Comment on the morphology of the erythrocytes.
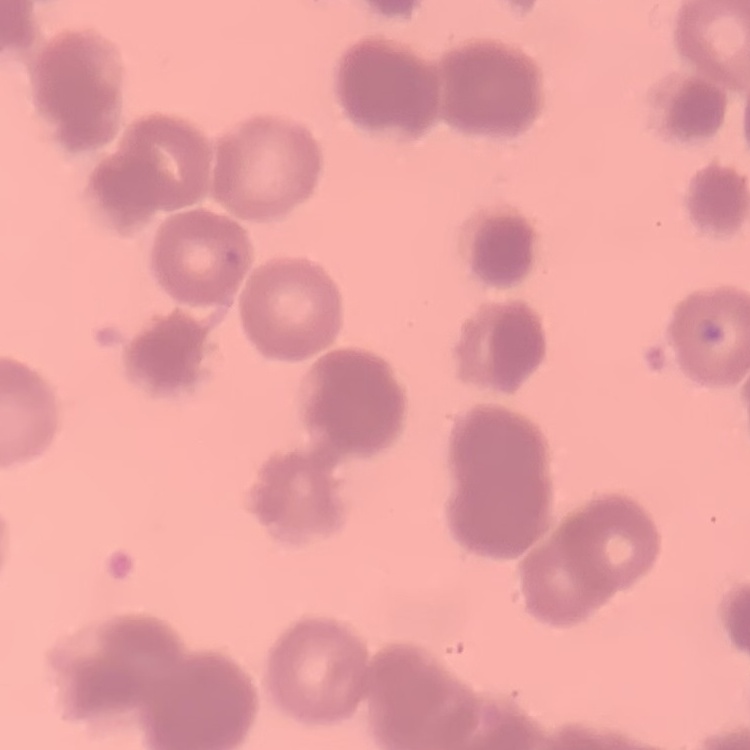
They show rouleaux formation.

stain = Field's or Giemsa
preparation = thin blood smear
image type = one tile cut from a larger photomicrograph